State the blood parasite species.
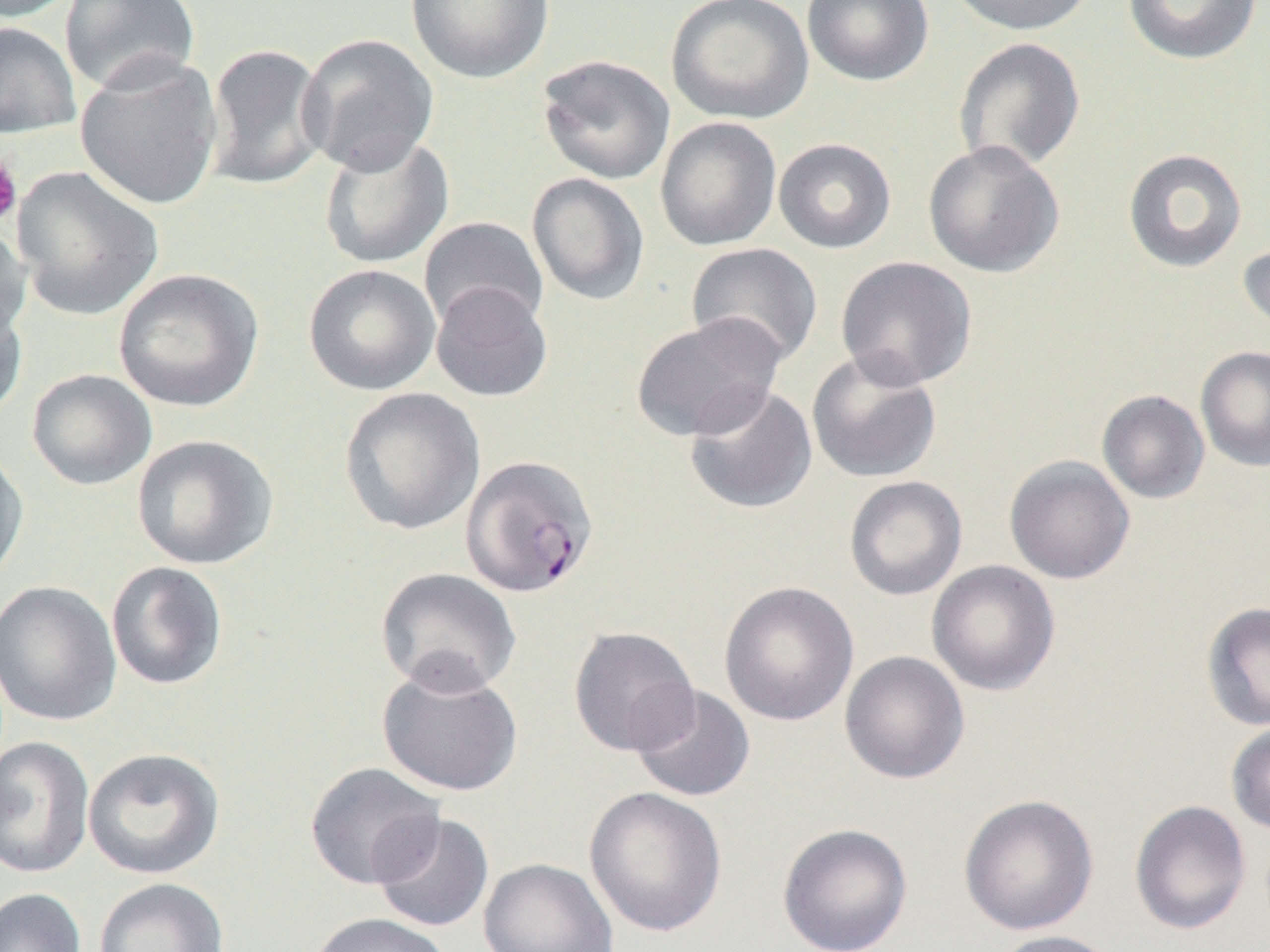
Plasmodium falciparum.

Approximate bounding boxes as named x1/y1/x2/y2 corners in pixels. Uninfected red blood cell locations: (x1=0, y1=0, x2=79, y2=22), (x1=59, y1=0, x2=201, y2=96), (x1=406, y1=0, x2=553, y2=84), (x1=665, y1=0, x2=814, y2=124), (x1=802, y1=0, x2=934, y2=87), (x1=944, y1=0, x2=1099, y2=36), (x1=1123, y1=0, x2=1263, y2=65), (x1=0, y1=21, x2=81, y2=140), (x1=297, y1=33, x2=441, y2=176), (x1=953, y1=37, x2=1086, y2=174), (x1=204, y1=42, x2=331, y2=192), (x1=74, y1=54, x2=223, y2=212), (x1=536, y1=54, x2=676, y2=185), (x1=655, y1=117, x2=782, y2=251), (x1=318, y1=132, x2=454, y2=270), (x1=773, y1=137, x2=896, y2=254), (x1=922, y1=140, x2=1065, y2=278), (x1=1123, y1=148, x2=1248, y2=273), (x1=11, y1=166, x2=163, y2=322), (x1=526, y1=172, x2=650, y2=306), (x1=420, y1=216, x2=549, y2=332), (x1=0, y1=220, x2=31, y2=344), (x1=1237, y1=238, x2=1270, y2=340), (x1=686, y1=242, x2=823, y2=367), (x1=835, y1=256, x2=978, y2=391), (x1=303, y1=264, x2=440, y2=396), (x1=113, y1=268, x2=263, y2=412), (x1=430, y1=282, x2=553, y2=403), (x1=0, y1=291, x2=29, y2=424), (x1=629, y1=313, x2=784, y2=442), (x1=1196, y1=346, x2=1270, y2=472), (x1=806, y1=350, x2=942, y2=484), (x1=26, y1=369, x2=158, y2=491), (x1=684, y1=383, x2=818, y2=515), (x1=339, y1=387, x2=485, y2=536), (x1=1096, y1=389, x2=1210, y2=504), (x1=131, y1=434, x2=279, y2=571), (x1=0, y1=443, x2=30, y2=589), (x1=1004, y1=455, x2=1135, y2=585), (x1=844, y1=476, x2=967, y2=601), (x1=926, y1=560, x2=1061, y2=696), (x1=106, y1=561, x2=228, y2=691), (x1=375, y1=567, x2=522, y2=696), (x1=0, y1=580, x2=122, y2=727), (x1=718, y1=581, x2=860, y2=726), (x1=1202, y1=601, x2=1270, y2=731), (x1=568, y1=626, x2=700, y2=757), (x1=839, y1=650, x2=970, y2=785), (x1=376, y1=662, x2=524, y2=797), (x1=629, y1=684, x2=756, y2=803), (x1=1226, y1=721, x2=1270, y2=835), (x1=0, y1=736, x2=96, y2=879), (x1=83, y1=747, x2=225, y2=879), (x1=304, y1=761, x2=445, y2=890), (x1=584, y1=786, x2=727, y2=938), (x1=958, y1=794, x2=1099, y2=936), (x1=1129, y1=800, x2=1252, y2=935), (x1=371, y1=813, x2=494, y2=933), (x1=777, y1=823, x2=912, y2=952), (x1=478, y1=857, x2=618, y2=952), (x1=94, y1=877, x2=230, y2=952), (x1=0, y1=887, x2=86, y2=952), (x1=306, y1=912, x2=453, y2=952), (x1=988, y1=929, x2=1123, y2=952). Plasmodium falciparum-infected red blood cell locations: (x1=460, y1=454, x2=599, y2=598). Platelet locations: (x1=0, y1=152, x2=23, y2=227). Thin blood smear. Optical microscopy. One field of a larger specimen. Image is 1270×952 pixels. 1000x magnification.